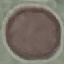

{
  "result": "no malaria parasites seen",
  "image_type": "automatically extracted cell patch, resized to 64 × 64 pixels",
  "capture": "smartphone through the microscope eyepiece",
  "preparation": "thin blood smear",
  "stain": "Giemsa"
}